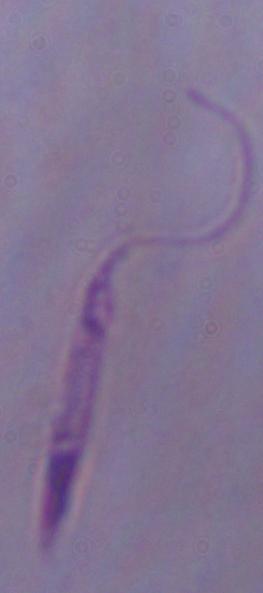

Summary:
  - Modality: photomicrograph
  - Magnification: 1000x
  - Identification: Leishmania